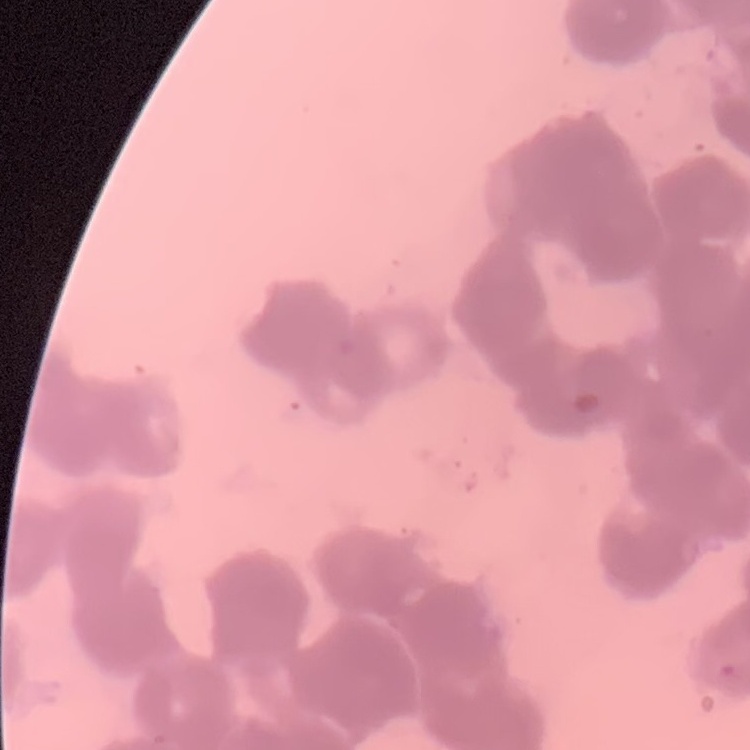

Summary:
  - Erythrocyte morphology: rouleaux formation
  - Image type: one tile cut from a larger photomicrograph
  - Stain: Field's or Giemsa
  - Preparation: thin peripheral smear